Identify the parasite.
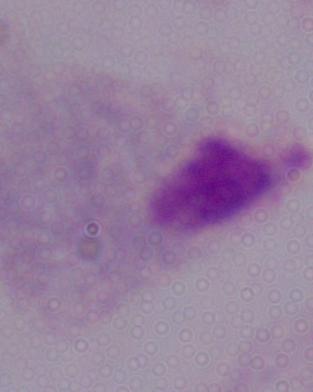

A trichomonad.

Micrograph. Captured at 1000x magnification.